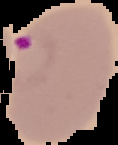

image size = 118×145 pixels
image type = segmented cell region with the area outside set to black
malaria status = parasitized
preparation = thin blood smear